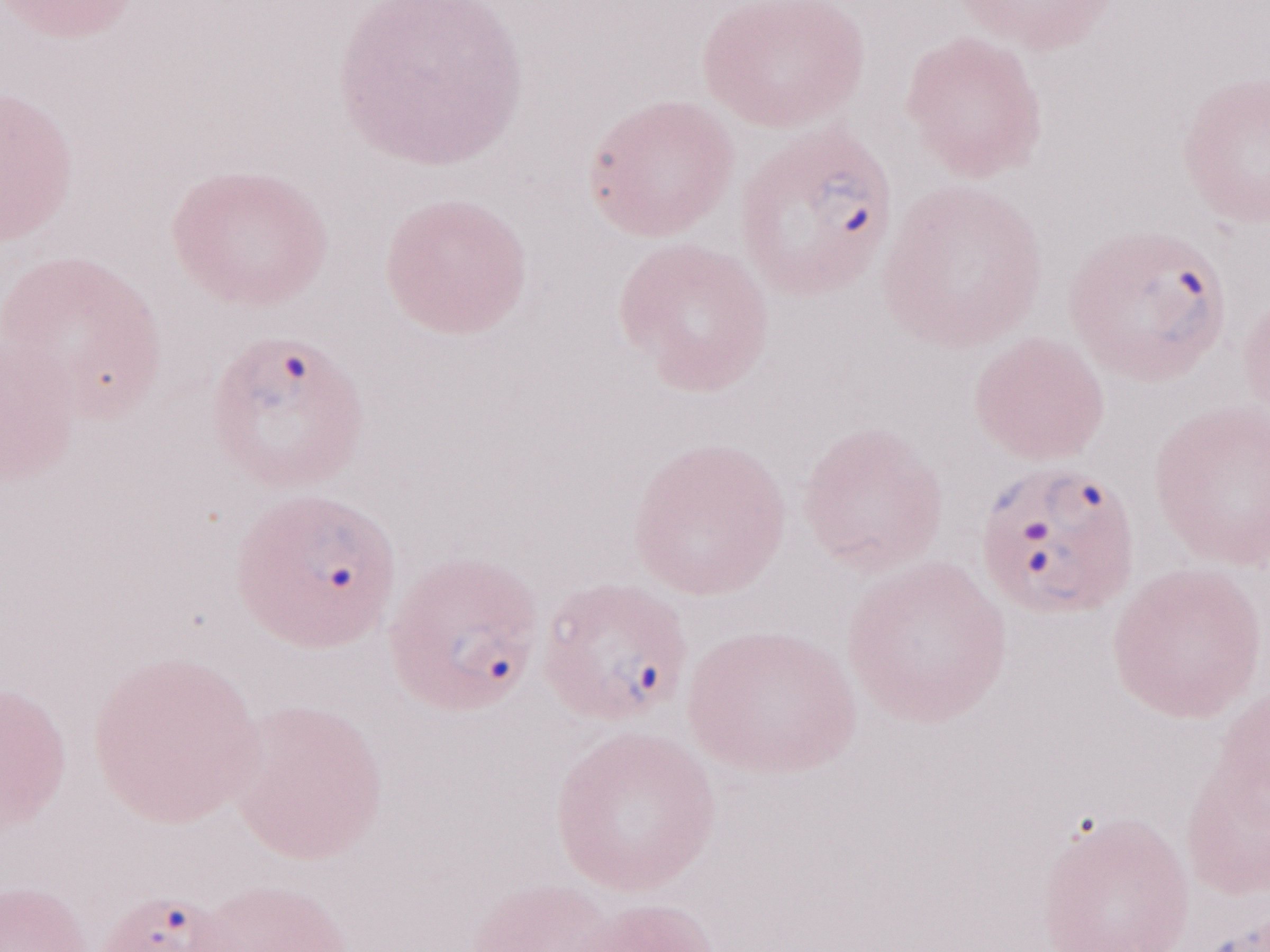

1,000x magnification. Image is 1270×952 pixels. Patient diagnosis: malaria infection. May-Grünwald-Giemsa-stained preparation. One field of this slide. Thin blood film. Olympus BX43 microscope, Olympus DP73 camera.